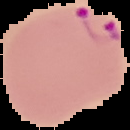
Summary:
  - Image size: 130×130 pixels
  - Malaria status: parasitized
  - Preparation: thin blood smear
  - Image type: cell region segmented out of the field of view; surrounding area masked to black